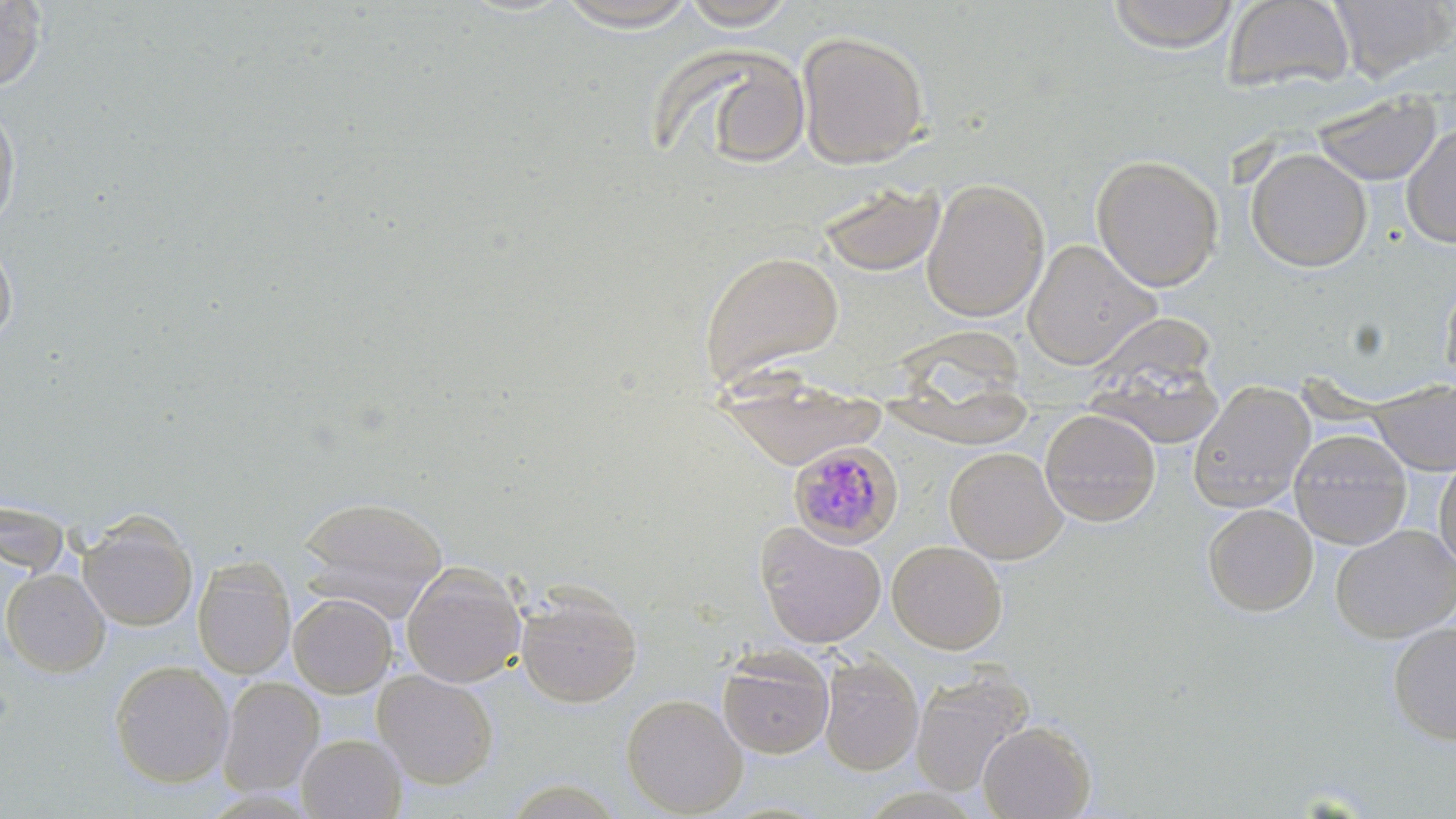
Approximate bounding boxes as named x1/y1/x2/y2 corners in pixels. Plasmodium malariae-infected red blood cell locations: (x1=788, y1=441, x2=904, y2=549). Uninfected red blood cell locations: (x1=1107, y1=0, x2=1239, y2=53), (x1=1222, y1=0, x2=1355, y2=95), (x1=1330, y1=0, x2=1454, y2=81), (x1=0, y1=1, x2=46, y2=90), (x1=552, y1=1, x2=703, y2=32), (x1=680, y1=1, x2=799, y2=30), (x1=796, y1=29, x2=930, y2=168), (x1=683, y1=47, x2=814, y2=170), (x1=1312, y1=91, x2=1441, y2=186), (x1=0, y1=103, x2=21, y2=233), (x1=1401, y1=122, x2=1456, y2=248), (x1=1246, y1=148, x2=1372, y2=272), (x1=1091, y1=153, x2=1224, y2=292), (x1=921, y1=178, x2=1049, y2=322), (x1=818, y1=181, x2=946, y2=277), (x1=1022, y1=239, x2=1159, y2=369), (x1=0, y1=241, x2=17, y2=343), (x1=698, y1=249, x2=846, y2=387), (x1=1440, y1=272, x2=1456, y2=392), (x1=885, y1=310, x2=1036, y2=450), (x1=1082, y1=343, x2=1226, y2=451), (x1=716, y1=366, x2=886, y2=470), (x1=1188, y1=379, x2=1315, y2=513), (x1=1371, y1=380, x2=1456, y2=476), (x1=1040, y1=408, x2=1161, y2=527), (x1=1288, y1=428, x2=1413, y2=549), (x1=944, y1=446, x2=1067, y2=563), (x1=1434, y1=456, x2=1456, y2=573), (x1=295, y1=495, x2=449, y2=620), (x1=0, y1=499, x2=70, y2=577), (x1=1202, y1=503, x2=1318, y2=616), (x1=78, y1=514, x2=197, y2=632), (x1=754, y1=521, x2=886, y2=649), (x1=1331, y1=524, x2=1456, y2=643), (x1=887, y1=540, x2=1007, y2=654), (x1=192, y1=558, x2=296, y2=680), (x1=401, y1=561, x2=527, y2=688), (x1=1, y1=568, x2=109, y2=676), (x1=515, y1=585, x2=642, y2=708), (x1=288, y1=592, x2=398, y2=697), (x1=1387, y1=622, x2=1456, y2=744), (x1=717, y1=647, x2=835, y2=760), (x1=817, y1=656, x2=923, y2=775), (x1=109, y1=660, x2=234, y2=787), (x1=372, y1=669, x2=498, y2=790), (x1=910, y1=669, x2=1034, y2=797), (x1=217, y1=677, x2=324, y2=797), (x1=621, y1=693, x2=748, y2=817), (x1=977, y1=720, x2=1096, y2=819), (x1=296, y1=732, x2=407, y2=818). Slide-level diagnosis: Plasmodium malariae. Image is 1456×819 pixels. Light microscopy. 1000x magnification. May-Grünwald-Giemsa stain. Thin blood film. Single field of view.